State which cell type is depicted.
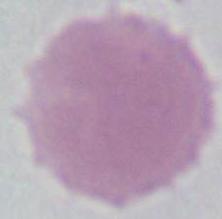
This is an erythrocyte.

Summary:
  - Magnification: 1000x
  - Modality: micrograph